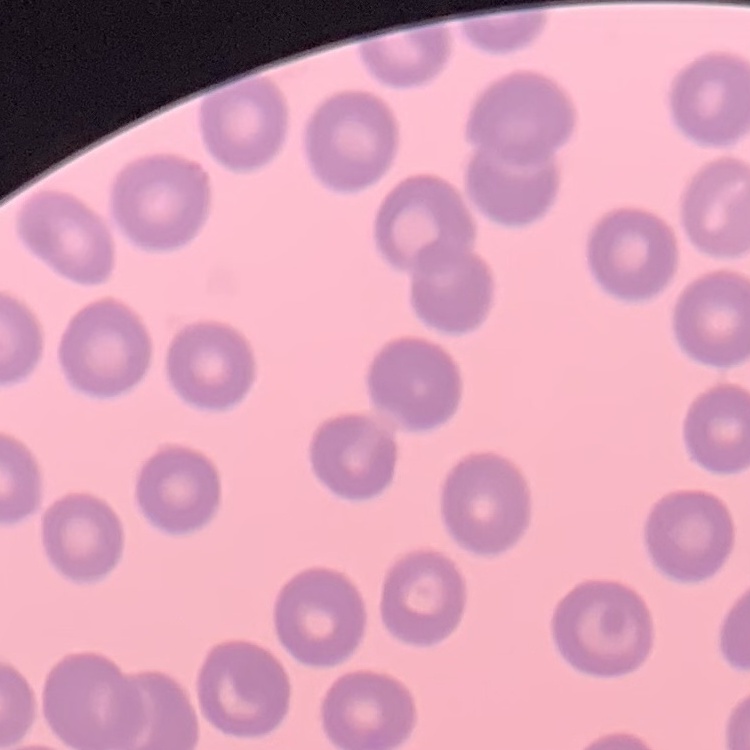

Summary:
  - Red blood cell morphology: no rouleaux formation
  - Preparation: thin blood smear
  - Stain: Field's or Giemsa
  - Image type: square crop of a larger photomicrograph